Assess this cell for malaria.
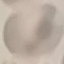

Uninfected.

Giemsa stain. Thin blood smear. Cell patch, automatically extracted from a larger field of view and resized to 64 × 64 pixels. Acquired by smartphone through the microscope eyepiece.